Locate and identify every blood parasite.
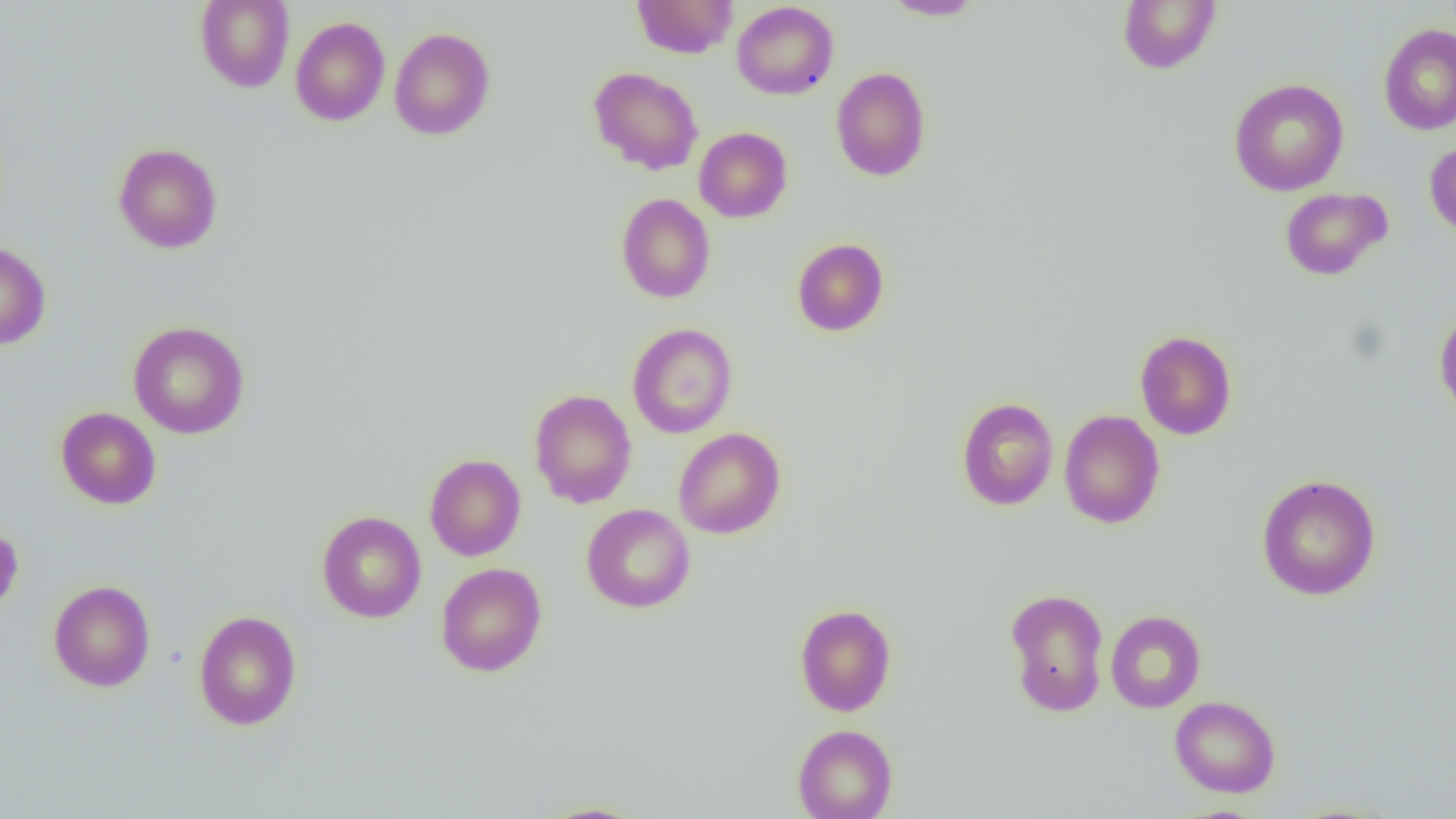
No blood parasites observed.

Approximate bounding boxes as (x1,y1)-(x2,y2) corner pairs in pixels. Uninfected red blood cell locations: (195,0)-(294,92), (631,0)-(738,58), (1117,0)-(1222,75), (732,1)-(839,100), (880,1)-(986,20), (290,16)-(390,126), (1378,24)-(1456,136), (389,27)-(495,140), (588,66)-(703,175), (831,66)-(931,181), (1229,78)-(1349,196), (694,127)-(792,223), (1425,139)-(1456,240), (112,143)-(223,254), (1280,187)-(1392,280), (616,193)-(716,303), (792,238)-(889,336), (0,240)-(51,350), (1434,306)-(1456,425), (128,320)-(250,439), (627,323)-(737,438), (1135,330)-(1237,440), (529,389)-(637,508), (956,396)-(1059,510), (56,407)-(161,509), (1058,409)-(1165,529), (673,427)-(786,539), (424,454)-(526,561), (1256,474)-(1381,600), (581,503)-(696,613), (316,510)-(427,623), (0,521)-(23,619), (436,562)-(547,677), (48,579)-(155,691), (1004,588)-(1110,717), (794,604)-(896,716), (193,609)-(302,731), (1105,610)-(1206,713), (1170,695)-(1281,797), (792,724)-(898,819), (534,801)-(651,818). Slide-level diagnosis: negative for blood parasites. Optical microscopy. Captured at 1000x magnification. Image is 1456×819 pixels. Single field of view. Thin blood film.